Classify this cell by malaria status.
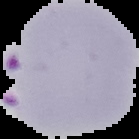
Parasitized.

Summary:
  - Image size: 139×139 pixels
  - Preparation: thin blood film
  - Image type: segmented cell region with the area outside set to black